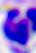 Micrograph. A leukocyte is shown. 400x magnification.